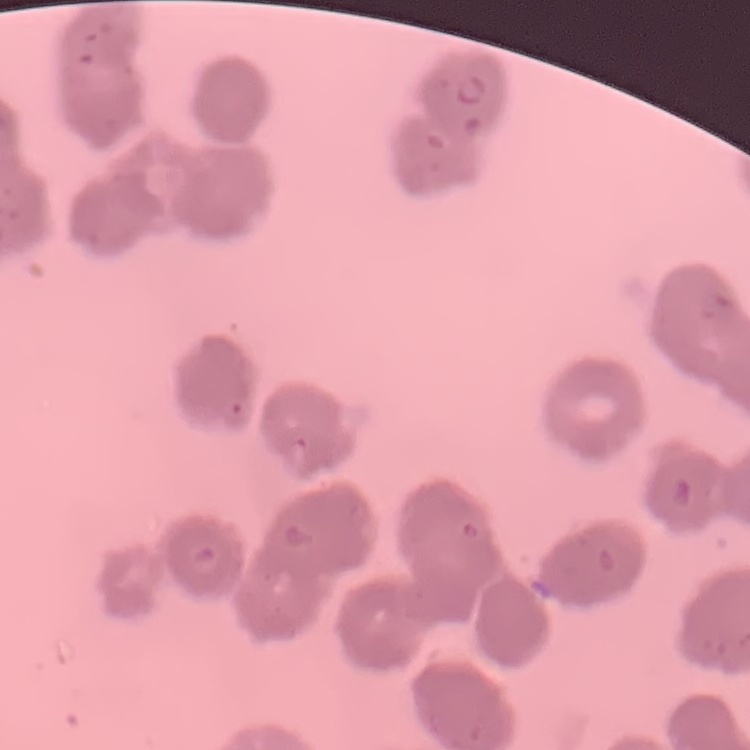

{
  "erythrocyte_morphology": "rouleaux formation",
  "image_type": "one tile cut from a larger photomicrograph",
  "stain": "Field's or Giemsa",
  "preparation": "thin peripheral smear"
}